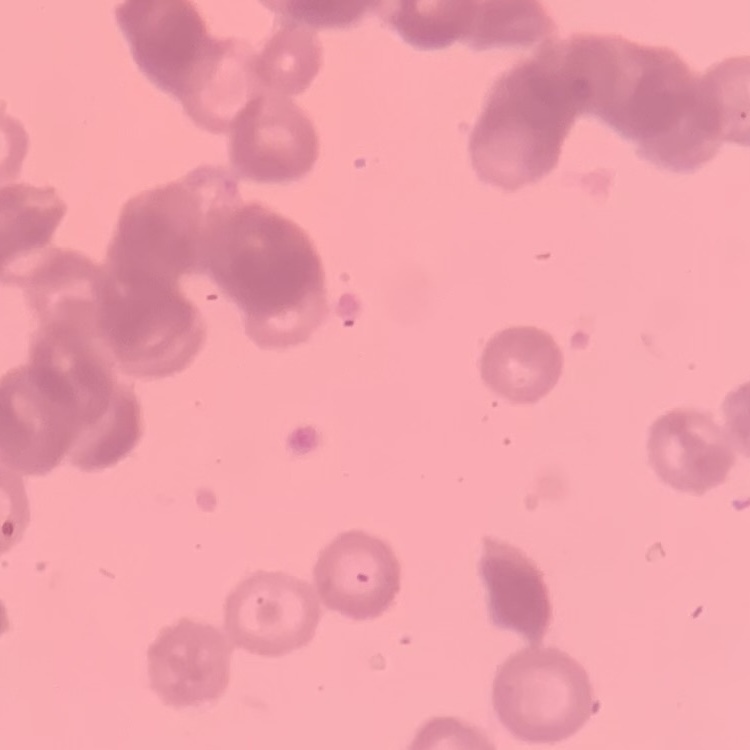

The red blood cells exhibit rouleaux formation. Thin peripheral smear. Stained with either Field's or Giemsa. Square crop of a larger photomicrograph.